Look for Plasmodium parasites.
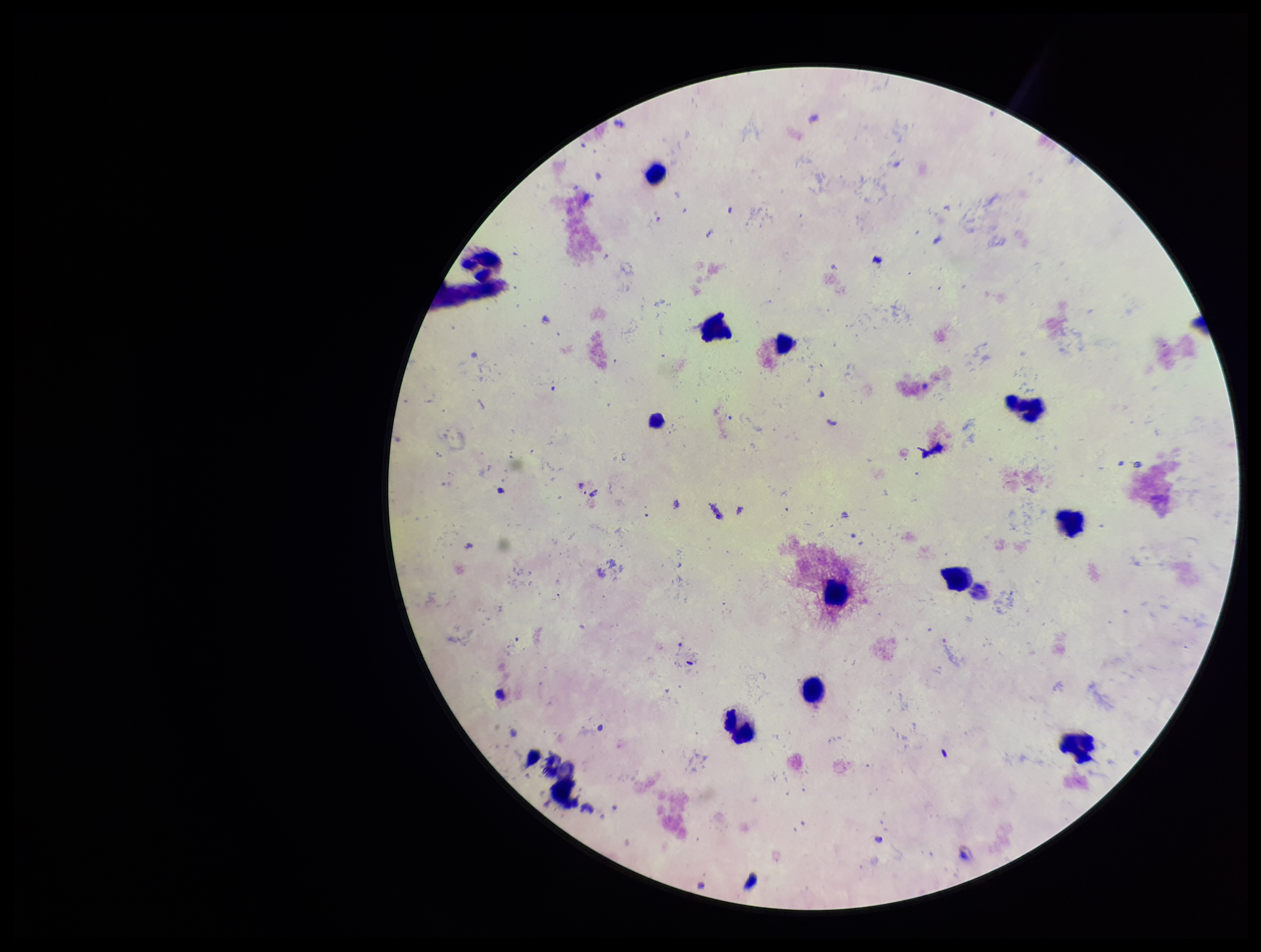

None identified.

Leukocyte count: 11. Stained with Giemsa. Smartphone photograph taken through the eyepiece of a microscope. Single field of view. Image is 1261×952 pixels. Preparation: thick. Patient malaria status: negative. Parasite count: 0.